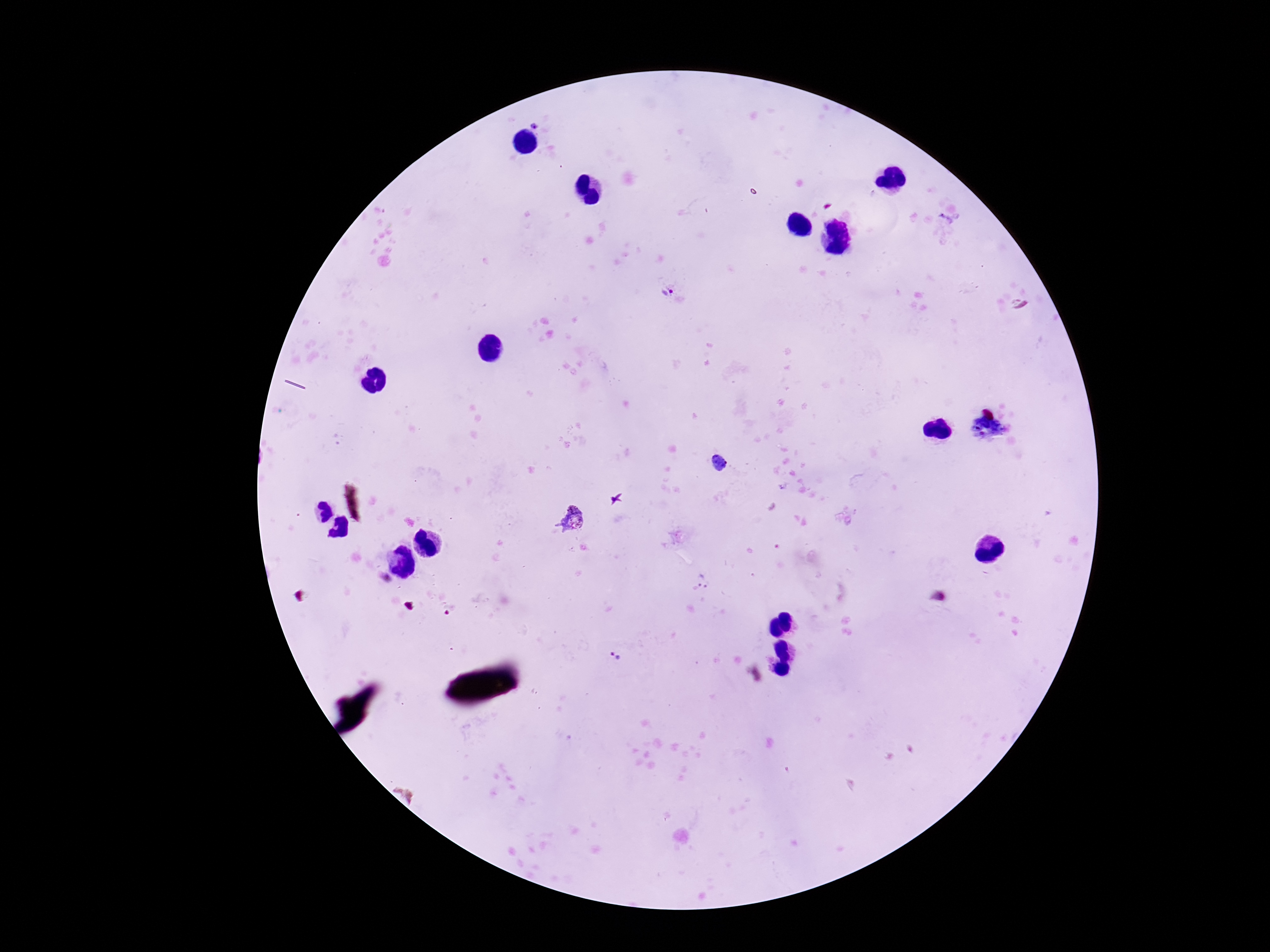

Approximate centers as (x, y) in pixels.
Summary:
  - Plasmodium parasite locations: (947, 225), (666, 290), (718, 461), (572, 517), (618, 657)
  - Field of view: single
  - Magnification: 100x
  - Preparation: thick blood smear
  - Image size: 1270×952 pixels
  - Stain: Giemsa
  - Patient malaria status: positive
  - Capture: smartphone camera through the microscope eyepiece